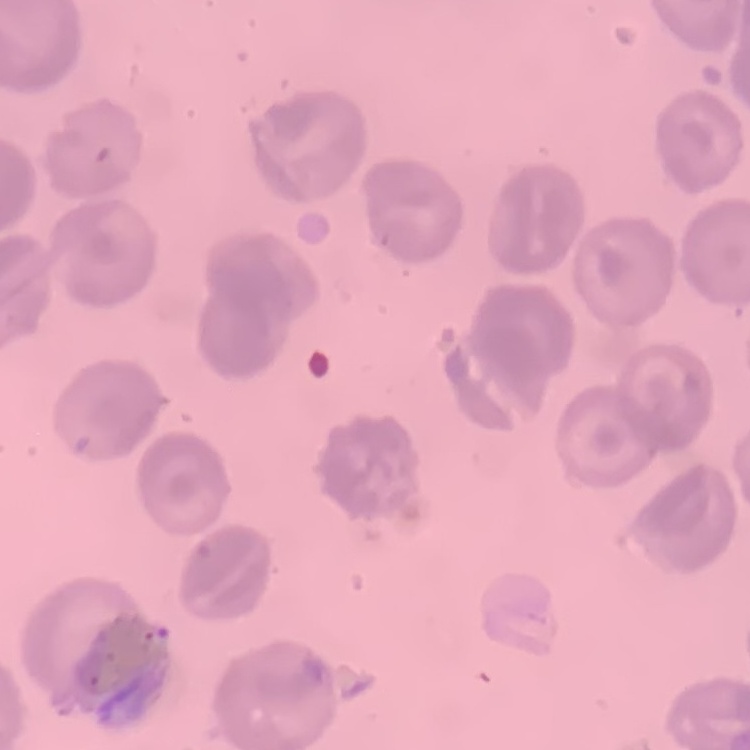
Summary:
  - Erythrocyte morphology: no rouleaux formation
  - Stain: Field's or Giemsa
  - Preparation: thin blood smear
  - Image type: one tile cut from a larger photomicrograph